Identify the blood parasite species.
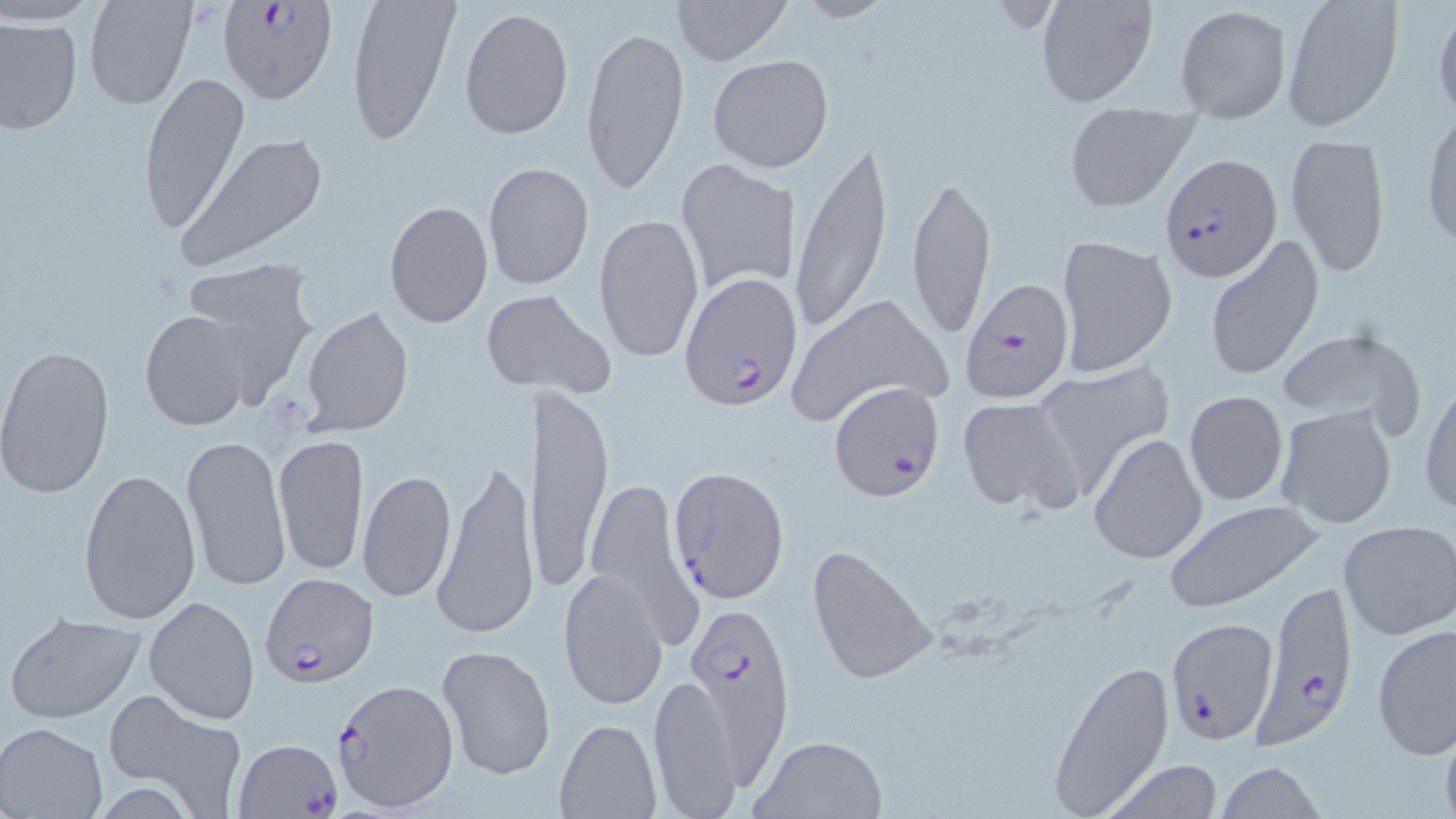
Plasmodium falciparum.

Approximate bounding boxes as [x1, y1, x2, y2] in pixels. Plasmodium falciparum-infected red blood cell locations: [216, 0, 339, 105], [1163, 154, 1282, 282], [679, 272, 803, 409], [960, 279, 1074, 403], [829, 378, 945, 501], [667, 464, 789, 605], [258, 572, 379, 686], [1249, 580, 1358, 750], [681, 599, 794, 767], [1167, 618, 1280, 745], [330, 679, 459, 811], [234, 737, 343, 817]. Uninfected red blood cell locations: [82, 0, 197, 111], [345, 0, 461, 145], [671, 0, 791, 66], [790, 0, 896, 25], [1033, 0, 1161, 109], [1281, 0, 1402, 132], [1431, 1, 1456, 119], [1175, 4, 1291, 122], [458, 6, 574, 140], [0, 15, 82, 135], [578, 23, 689, 199], [707, 53, 835, 173], [137, 71, 250, 234], [1063, 104, 1198, 213], [1420, 116, 1456, 252], [176, 133, 330, 268], [1282, 133, 1390, 278], [789, 136, 896, 340], [674, 158, 801, 297], [482, 161, 594, 290], [907, 173, 997, 338], [384, 198, 494, 327], [593, 213, 705, 363], [1055, 234, 1179, 376], [1206, 236, 1326, 383], [182, 259, 318, 396], [502, 291, 618, 402], [783, 292, 954, 428], [300, 306, 413, 436], [140, 312, 250, 430], [1275, 324, 1428, 438], [0, 345, 115, 499], [1031, 363, 1174, 495], [1420, 378, 1455, 518], [530, 383, 614, 596], [1182, 391, 1291, 507], [955, 396, 1083, 515], [1274, 404, 1401, 531], [181, 430, 290, 596], [272, 432, 370, 578], [1089, 433, 1208, 565], [431, 453, 539, 641], [358, 466, 458, 603], [78, 468, 201, 626], [582, 478, 702, 644], [1163, 498, 1327, 613], [1336, 520, 1455, 642], [806, 543, 938, 687], [557, 568, 670, 710], [144, 595, 261, 725], [5, 609, 147, 724], [1372, 624, 1456, 759], [436, 643, 558, 780], [1047, 657, 1175, 818], [648, 674, 741, 817], [103, 689, 248, 817], [554, 718, 661, 818], [1, 722, 107, 818], [751, 733, 887, 818], [1097, 760, 1229, 818], [1215, 763, 1329, 819]. Image is 1456×819 pixels. Captured at 1000x magnification. May-Grünwald-Giemsa-stained preparation. Thin blood film. Optical microscopy. One field of a larger specimen.